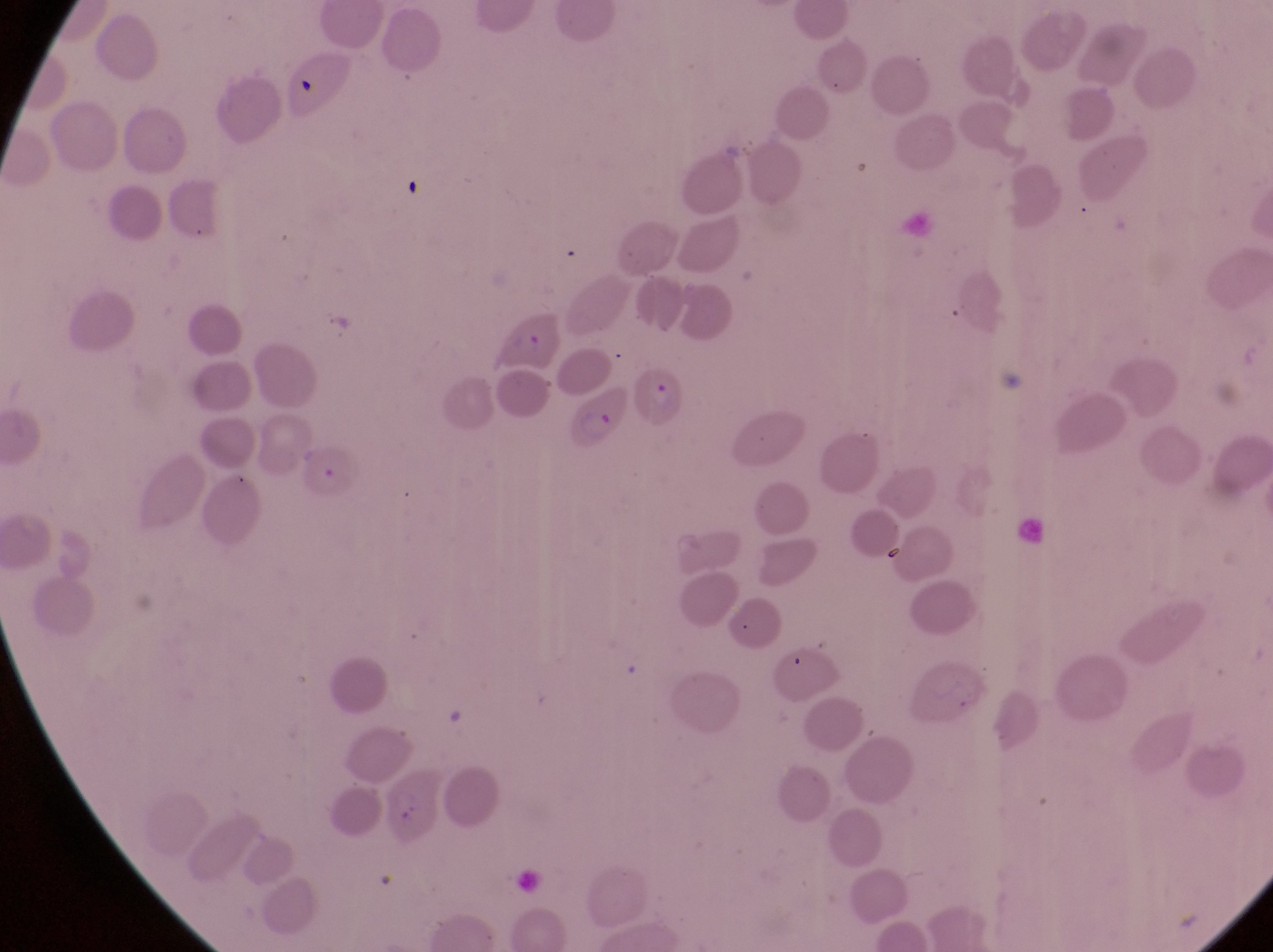
Approximate bounding boxes as left top right bottom in pixels.
Summary:
  - Parasitised red blood cell locations: 486 307 566 372; 637 364 697 438; 569 387 632 455; 304 440 364 500
  - Capture: smartphone photograph through the eyepiece of an Olympus CX-23 microscope
  - Country: Uganda
  - Image size: 1273×952 pixels
  - Preparation: thin blood smear
  - Field of view: single
  - Magnification: 1000x